Identify the parasite.
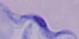

A trypanosome.

Photomicrograph. Captured at 1000x magnification.